Draw a bounding box around every malaria parasite, every leukocyte, and every artifact (stain precipitate or debris).
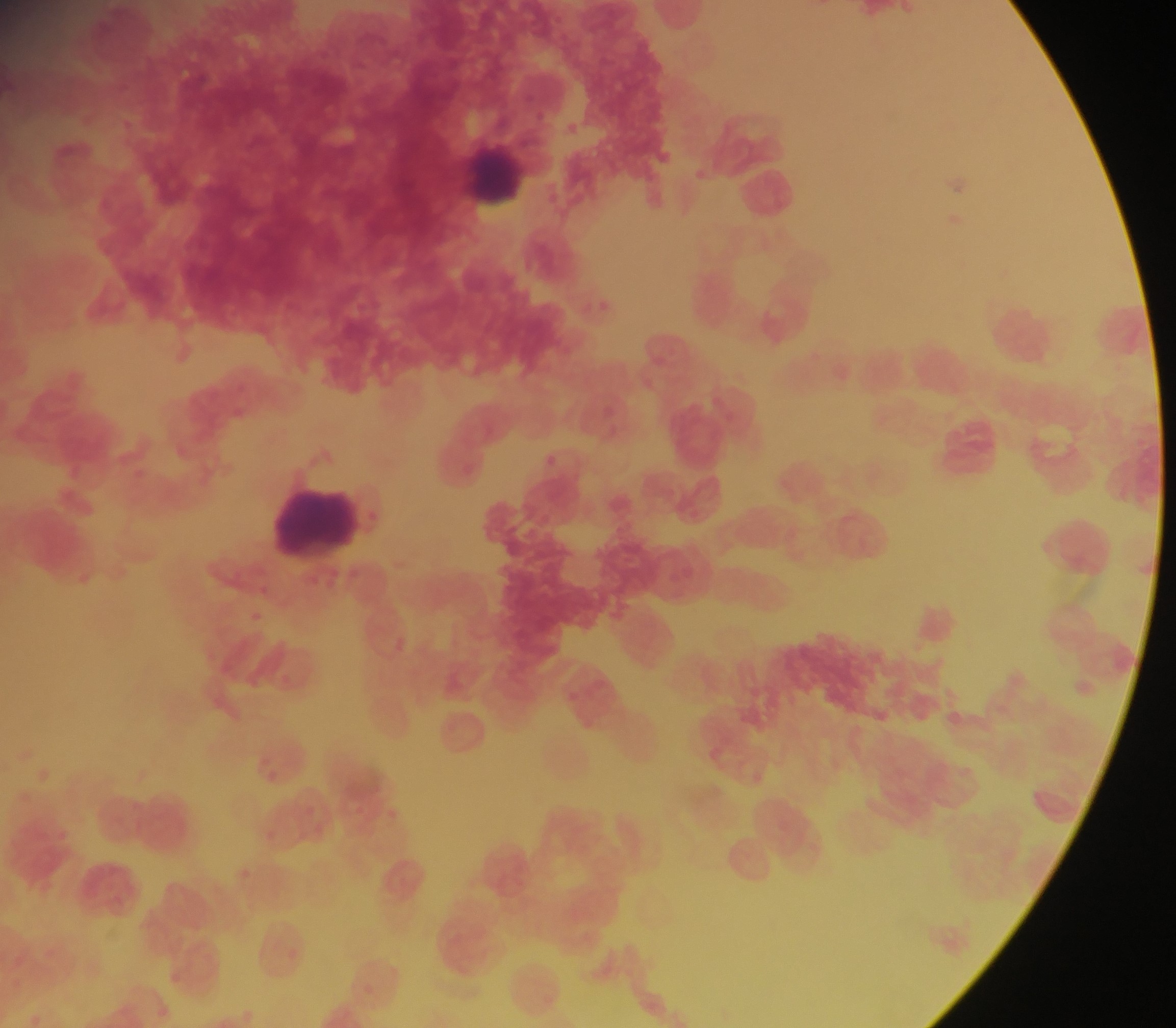

Approximate bounding boxes as [left, top, right, bottom] in pixels.
No malaria parasites observed.
Leukocytes: [456, 141, 532, 222], [732, 161, 800, 227], [983, 301, 1061, 368], [263, 484, 369, 563], [1044, 515, 1121, 588].

{
  "capture": "mobile-phone photograph through a microscope",
  "country": "Ghana",
  "preparation": "thin blood smear",
  "image_size": "1176×1028 pixels",
  "field_of_view": "single"
}